Comment on the morphology of the red blood cells.
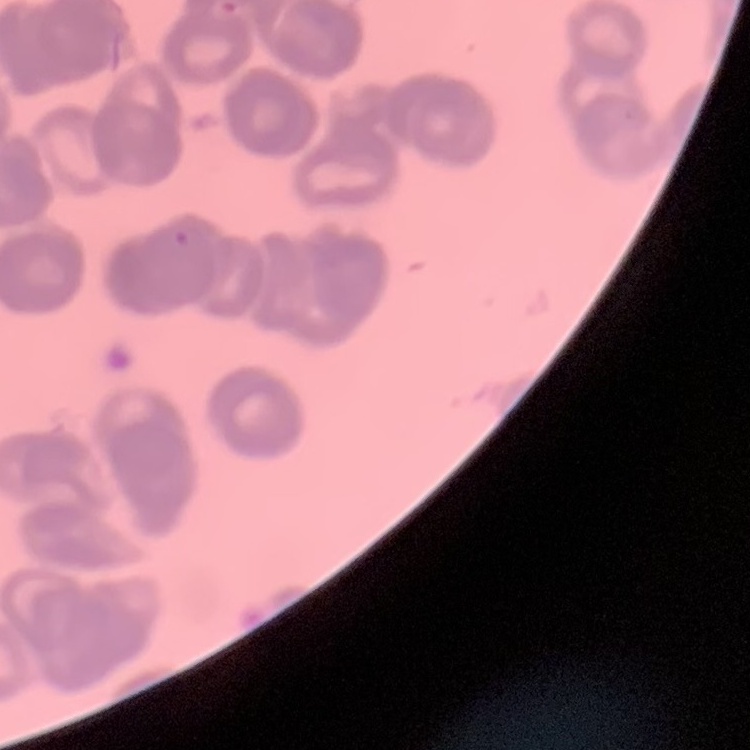

Rouleaux formation.

One tile cut from a larger photomicrograph. Field's or Giemsa stain. Thin peripheral smear.